Name the cell type shown.
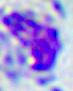
A leukocyte.

magnification = 400x
modality = micrograph